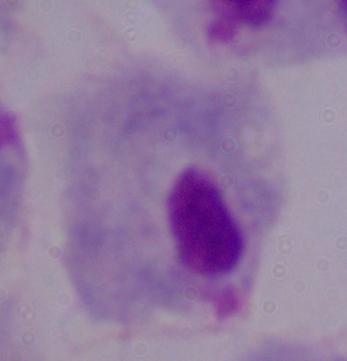

A trichomonad is shown. Captured at 1000x magnification. Photomicrograph.